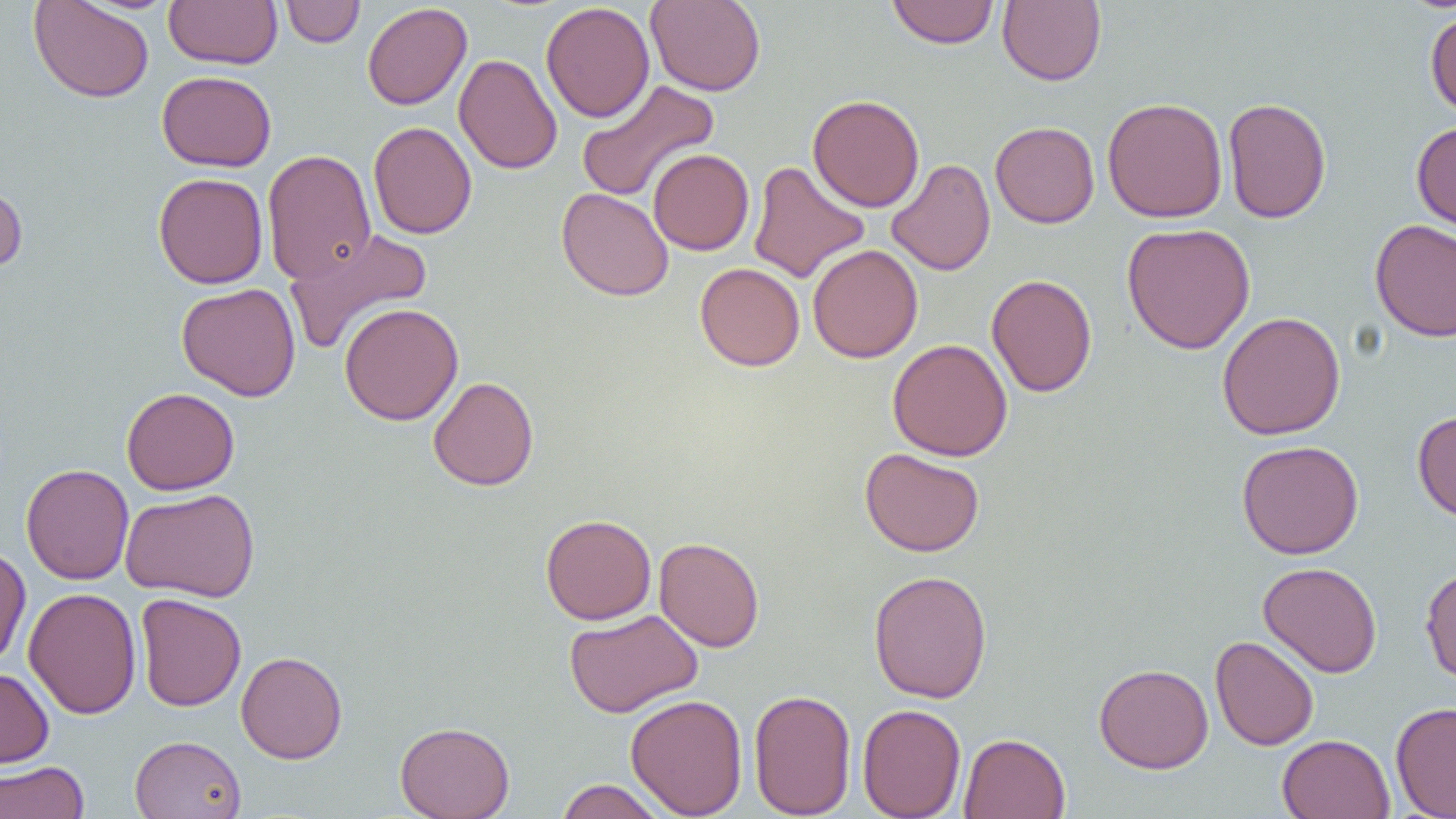

Approximate bounding boxes as (x1,y1)-(x2,y2) corner pairs in pixels. Uninfected red blood cell locations: (27,0)-(154,103), (163,0)-(283,69), (280,0)-(365,48), (886,0)-(999,49), (998,0)-(1107,86), (646,1)-(766,96), (362,2)-(472,110), (541,2)-(655,123), (1424,8)-(1456,119), (454,53)-(562,175), (156,70)-(277,172), (576,79)-(720,203), (807,94)-(925,212), (1102,96)-(1228,222), (1222,97)-(1332,224), (368,121)-(477,239), (990,121)-(1100,228), (1411,121)-(1456,233), (262,148)-(376,285), (648,148)-(755,255), (886,158)-(996,276), (748,159)-(870,284), (153,172)-(268,289), (0,179)-(28,275), (557,188)-(674,301), (1370,219)-(1456,342), (1121,222)-(1256,354), (283,227)-(432,355), (807,244)-(923,363), (695,262)-(805,371), (987,274)-(1097,397), (176,283)-(301,401), (339,302)-(464,426), (1217,311)-(1346,440), (887,339)-(1013,461), (428,376)-(539,491), (121,387)-(239,495), (1412,409)-(1456,523), (1236,440)-(1364,559), (859,447)-(985,557), (21,463)-(134,585), (120,487)-(260,603), (540,514)-(656,625), (653,536)-(765,652), (0,545)-(31,668), (1258,561)-(1382,678), (1420,565)-(1456,686), (868,569)-(993,704), (23,587)-(141,719), (135,593)-(247,711), (564,609)-(703,718), (1210,635)-(1319,751), (235,650)-(348,764), (1094,663)-(1213,773), (0,667)-(54,768), (749,689)-(857,818), (625,694)-(748,818), (1390,701)-(1456,818), (856,703)-(966,818), (395,721)-(515,819), (959,732)-(1071,819), (130,734)-(247,819), (1277,734)-(1395,819), (0,761)-(90,819), (554,779)-(669,819). Slide-level diagnosis: negative for blood parasites. Single field of view. 1000x magnification. Image is 1456×819 pixels. Thin blood smear. Optical microscopy.